Identify the cell.
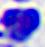

A leukocyte.

Summary:
  - Magnification: 400x
  - Modality: micrograph